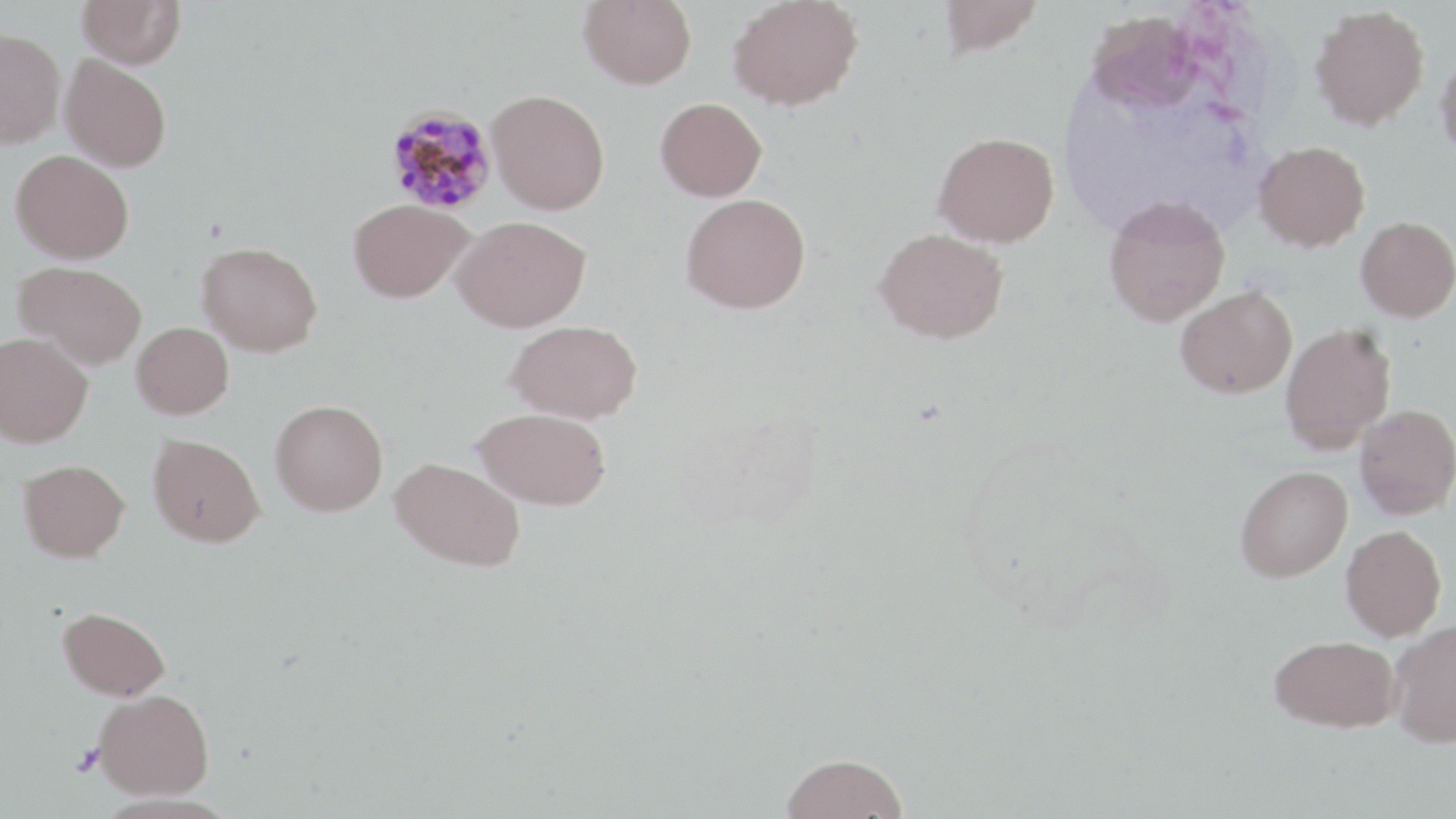

slide-level diagnosis = Plasmodium malariae
magnification = 1000x
preparation = thin blood film
uninfected red blood cell locations = approximate bounding boxes as (x1, y1, x2, y2) in pixels: (77, 0, 185, 69), (579, 0, 697, 89), (727, 0, 864, 111), (937, 0, 1045, 58), (1309, 4, 1430, 130), (1086, 9, 1205, 114), (0, 27, 66, 148), (1436, 49, 1456, 165), (60, 55, 172, 172), (487, 89, 610, 215), (655, 97, 767, 201), (933, 132, 1059, 247), (1254, 140, 1370, 252), (10, 149, 134, 263), (680, 193, 810, 314), (1103, 195, 1230, 326), (348, 199, 473, 302), (451, 215, 590, 332), (1356, 216, 1456, 321), (874, 227, 1008, 344), (196, 241, 323, 357), (13, 260, 147, 369), (1175, 286, 1297, 398), (506, 319, 642, 423), (132, 321, 234, 419), (1280, 323, 1396, 453), (0, 332, 93, 447), (270, 399, 388, 516), (1355, 404, 1456, 519), (473, 407, 612, 509), (148, 433, 265, 547), (390, 457, 525, 572), (18, 459, 129, 561), (1235, 465, 1352, 582), (1341, 525, 1446, 641), (57, 606, 171, 700), (1387, 619, 1456, 747), (1270, 634, 1400, 732), (94, 688, 214, 799), (780, 753, 909, 818)
field of view = one of a larger specimen
platelet locations = approximate bounding boxes as (x1, y1, x2, y2) in pixels: (72, 744, 107, 777)
stain = May-Grünwald-Giemsa
image size = 1456×819 pixels
Plasmodium malariae-infected red blood cell locations = approximate bounding boxes as (x1, y1, x2, y2) in pixels: (384, 105, 498, 215)
modality = optical microscopy